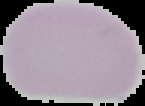

{
  "preparation": "thin blood film",
  "result": "no malaria parasites detected",
  "image_type": "segmented cell region on a black background",
  "image_size": "145×106 pixels"
}